Evaluate for Plasmodium parasites.
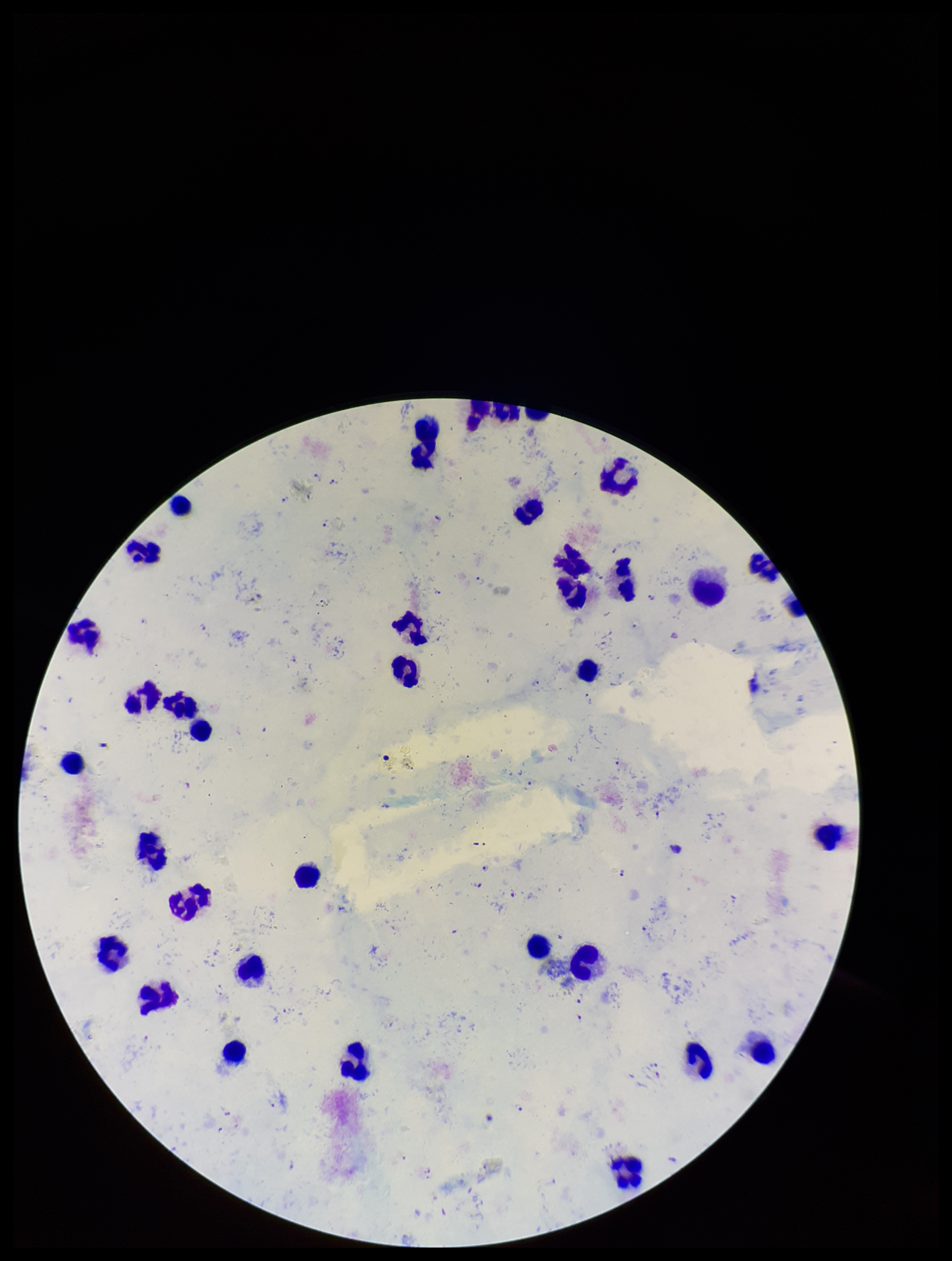

Identified.

Parasite count: 37. Leukocyte count: 35. Image is 952×1261 pixels. Preparation: thick. Photographed through the microscope eyepiece with a smartphone camera. Single field of view. Giemsa stain. Species reported for this patient: Plasmodium falciparum. Patient malaria status: positive.